Assess this cell for malaria.
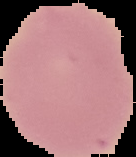
It is uninfected.

From a thin blood smear. Image is 136×157 pixels. Cell region segmented out of the field of view; the surrounding area is masked to black.